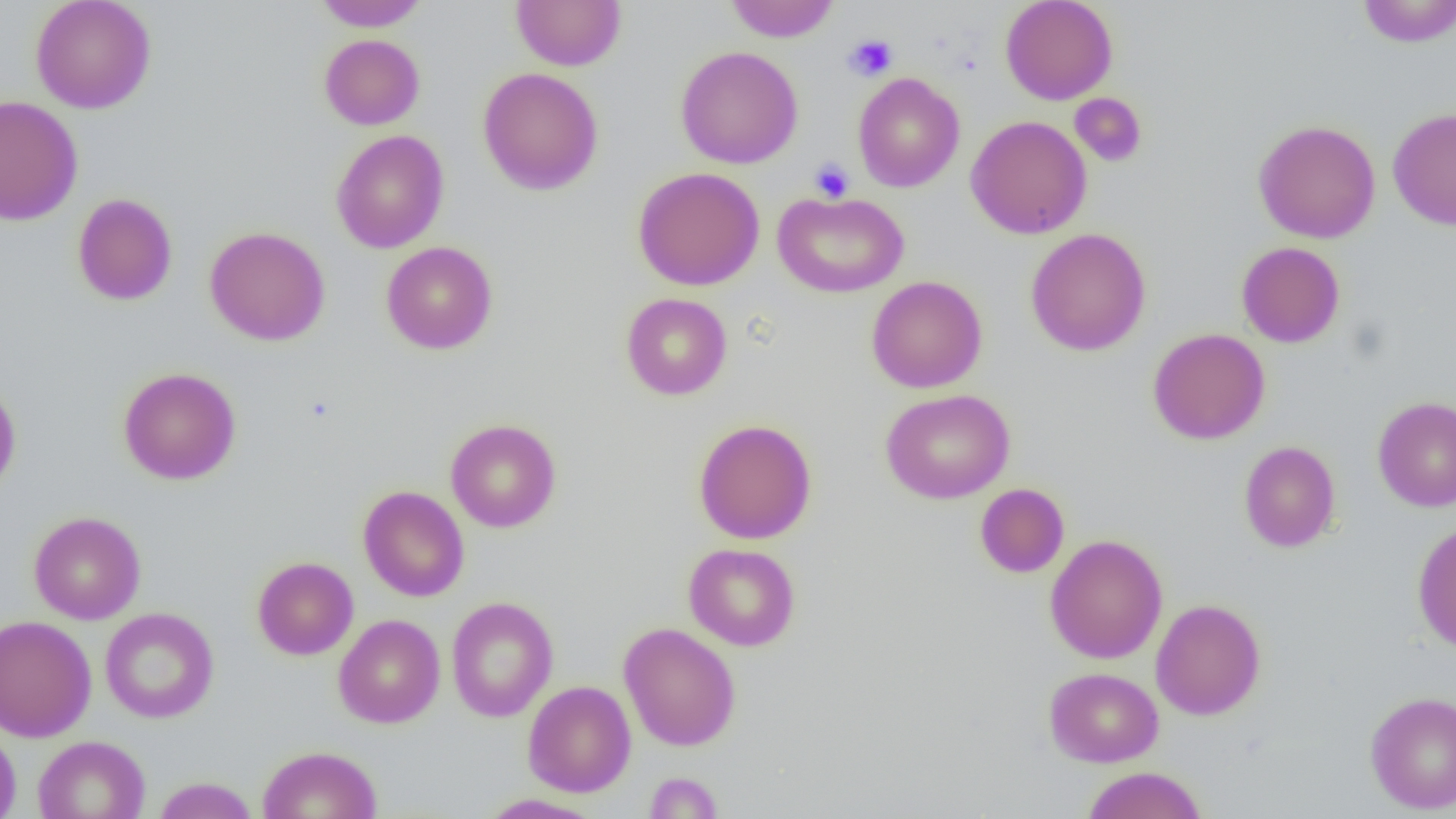
Summary:
  - Coordinate format: approximate bounding boxes as named x1/y1/x2/y2 corners in pixels
  - Uninfected red blood cell locations: (x1=30, y1=0, x2=157, y2=114), (x1=313, y1=0, x2=428, y2=31), (x1=511, y1=0, x2=626, y2=71), (x1=725, y1=0, x2=839, y2=42), (x1=999, y1=0, x2=1118, y2=104), (x1=1357, y1=0, x2=1456, y2=48), (x1=319, y1=34, x2=425, y2=130), (x1=675, y1=46, x2=803, y2=169), (x1=477, y1=67, x2=604, y2=195), (x1=852, y1=72, x2=965, y2=192), (x1=1070, y1=93, x2=1148, y2=166), (x1=0, y1=94, x2=83, y2=227), (x1=1388, y1=108, x2=1456, y2=231), (x1=966, y1=115, x2=1092, y2=239), (x1=1253, y1=119, x2=1381, y2=243), (x1=331, y1=130, x2=449, y2=254), (x1=632, y1=166, x2=765, y2=291), (x1=772, y1=191, x2=909, y2=298), (x1=72, y1=193, x2=178, y2=306), (x1=204, y1=226, x2=331, y2=346), (x1=1025, y1=228, x2=1151, y2=356), (x1=381, y1=241, x2=498, y2=354), (x1=1236, y1=241, x2=1345, y2=348), (x1=866, y1=276, x2=987, y2=393), (x1=621, y1=293, x2=732, y2=400), (x1=1147, y1=328, x2=1271, y2=445), (x1=118, y1=367, x2=241, y2=485), (x1=0, y1=380, x2=21, y2=499), (x1=880, y1=388, x2=1015, y2=504), (x1=1372, y1=395, x2=1456, y2=512), (x1=445, y1=418, x2=561, y2=533), (x1=693, y1=419, x2=817, y2=544), (x1=1239, y1=441, x2=1340, y2=553), (x1=975, y1=483, x2=1069, y2=578), (x1=358, y1=485, x2=469, y2=602), (x1=28, y1=511, x2=146, y2=625), (x1=1412, y1=521, x2=1456, y2=653), (x1=1045, y1=534, x2=1168, y2=664), (x1=683, y1=543, x2=800, y2=651), (x1=252, y1=557, x2=358, y2=660), (x1=446, y1=596, x2=559, y2=722), (x1=1151, y1=598, x2=1266, y2=720), (x1=100, y1=607, x2=219, y2=723), (x1=0, y1=614, x2=97, y2=742), (x1=333, y1=614, x2=446, y2=728), (x1=619, y1=622, x2=741, y2=751), (x1=1044, y1=667, x2=1163, y2=767), (x1=522, y1=680, x2=636, y2=797), (x1=1365, y1=690, x2=1456, y2=814), (x1=0, y1=725, x2=21, y2=819), (x1=33, y1=735, x2=150, y2=819), (x1=257, y1=745, x2=381, y2=819), (x1=1081, y1=767, x2=1207, y2=819), (x1=643, y1=771, x2=724, y2=818), (x1=152, y1=777, x2=259, y2=818), (x1=478, y1=793, x2=604, y2=818)
  - Platelet locations: (x1=844, y1=34, x2=898, y2=81), (x1=809, y1=158, x2=855, y2=203)
  - Slide-level diagnosis: negative for blood parasites
  - Field of view: one of a larger specimen
  - Modality: optical microscopy
  - Image size: 1456×819 pixels
  - Preparation: thin blood film
  - Magnification: 1000x